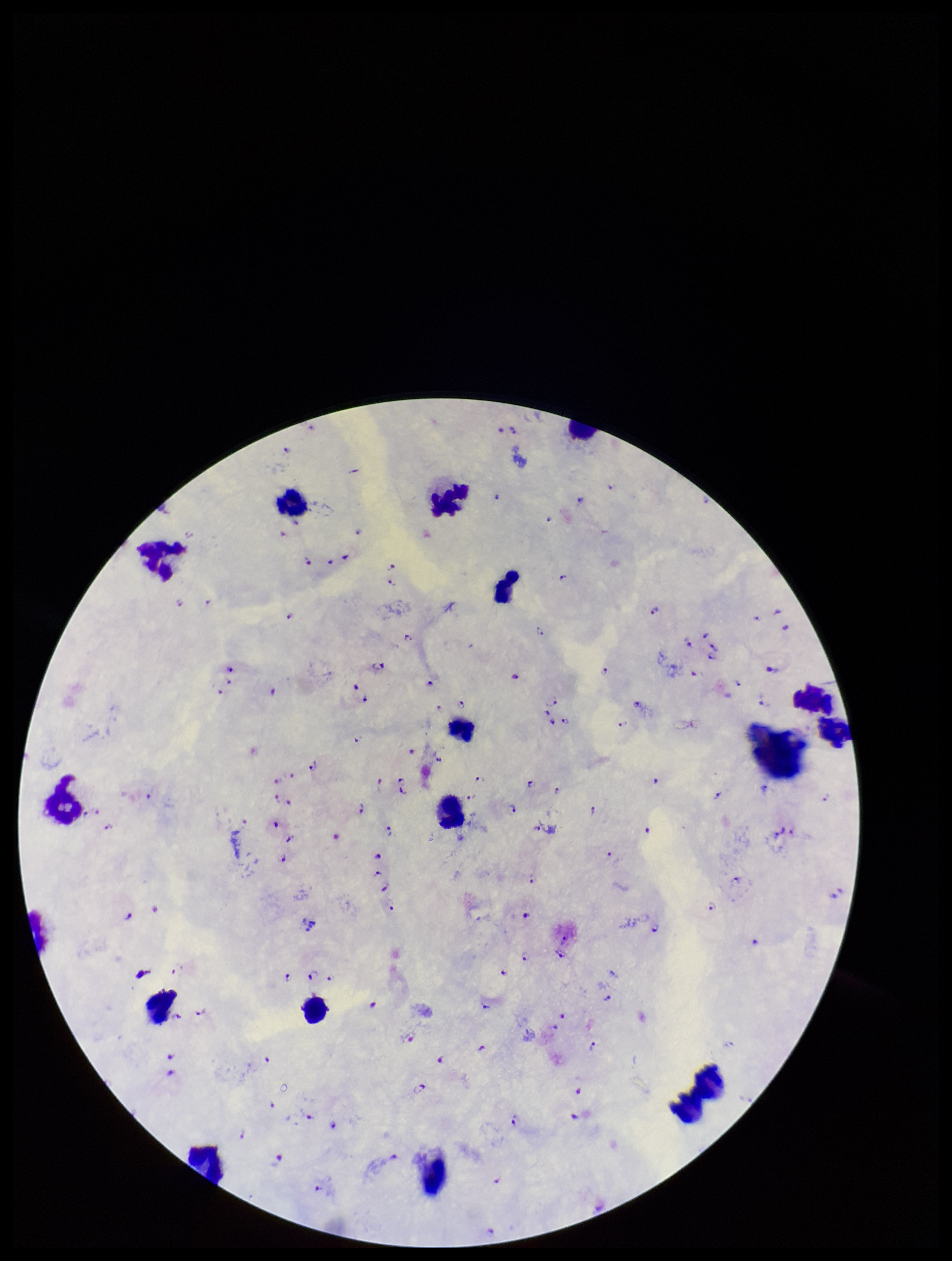

patient_malaria_status: positive
field_of_view: one from this slide
parasite_count: 121
stain: Giemsa
image_size: 952×1261 pixels
leukocyte_count: 17
capture: smartphone photograph through the microscope eyepiece
species_reported_for_this_patient: Plasmodium falciparum
plasmodium_parasites: identified
preparation: thick blood smear